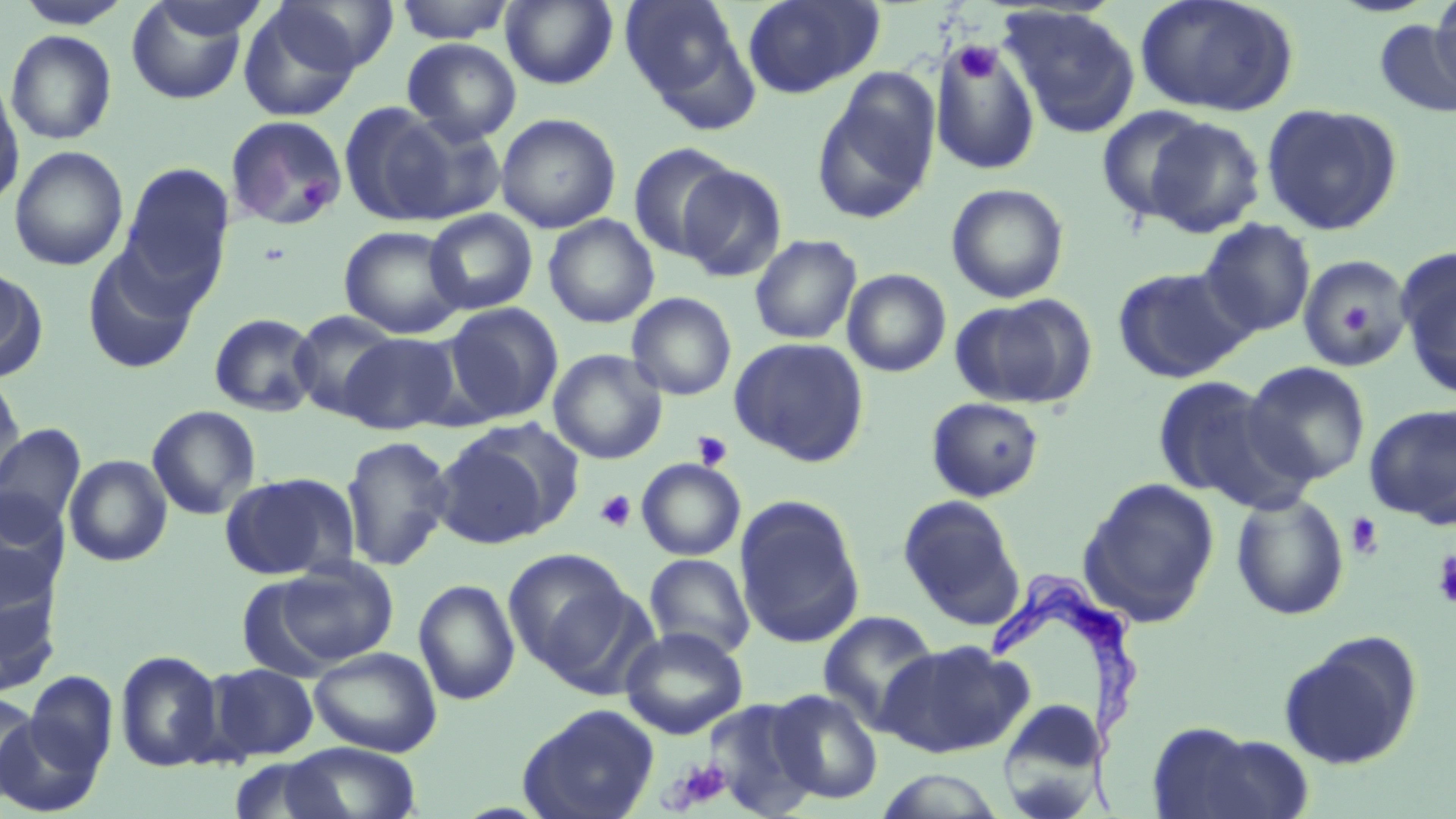
{
  "slide_level_diagnosis": "Trypanosoma brucei",
  "stain": "May-Grünwald-Giemsa",
  "image_size": "1456×819 pixels",
  "field_of_view": "one of a larger specimen",
  "modality": "light microscopy",
  "trypanosoma_brucei_locations": "approximate bounding boxes as [x1, y1, x2, y2] in pixels: [987, 569, 1151, 812]",
  "preparation": "thin blood film",
  "platelet_locations": "approximate bounding boxes as [x1, y1, x2, y2] in pixels: [953, 42, 1002, 84], [298, 175, 338, 211], [1340, 304, 1370, 334], [692, 430, 733, 470], [594, 489, 637, 533], [1345, 514, 1384, 559], [1431, 549, 1456, 609], [669, 758, 733, 810]",
  "magnification": "1000x",
  "uninfected_red_blood_cell_locations": "approximate bounding boxes as [x1, y1, x2, y2] in pixels: [14, 0, 134, 29], [147, 0, 272, 41], [393, 0, 516, 43], [501, 0, 618, 89], [620, 0, 753, 115], [742, 0, 884, 98], [1136, 0, 1297, 117], [1429, 0, 1456, 98], [125, 1, 254, 105], [270, 1, 398, 76], [238, 3, 363, 121], [1001, 5, 1141, 138], [1376, 19, 1456, 118], [4, 29, 117, 145], [402, 38, 522, 144], [931, 43, 1040, 176], [813, 74, 939, 224], [0, 76, 23, 210], [1261, 103, 1402, 235], [341, 104, 469, 226], [1095, 105, 1214, 224], [495, 113, 621, 233], [226, 115, 347, 230], [1144, 117, 1266, 238], [628, 142, 740, 261], [9, 145, 129, 271], [119, 162, 234, 297], [677, 164, 787, 282], [945, 183, 1069, 304], [424, 209, 538, 315], [543, 215, 659, 328], [1198, 219, 1316, 338], [338, 225, 466, 339], [749, 233, 862, 344], [82, 246, 201, 375], [1396, 250, 1456, 399], [1298, 252, 1414, 373], [0, 263, 46, 380], [1112, 265, 1253, 384], [842, 268, 952, 377], [627, 292, 737, 401], [951, 297, 1091, 408], [442, 303, 563, 424], [289, 310, 401, 419], [209, 312, 321, 417], [339, 333, 460, 434], [730, 336, 870, 466], [548, 349, 667, 464], [1242, 361, 1372, 486], [0, 371, 26, 495], [1150, 375, 1295, 506], [926, 397, 1045, 502], [1363, 402, 1456, 528], [146, 404, 261, 520], [0, 423, 87, 536], [435, 423, 575, 545], [340, 434, 455, 572], [64, 454, 172, 567], [637, 458, 746, 560], [219, 472, 359, 581], [1080, 478, 1220, 624], [1230, 490, 1350, 621], [0, 492, 69, 609], [898, 495, 1024, 628], [734, 496, 865, 648], [502, 547, 635, 678], [644, 554, 755, 660], [274, 557, 399, 667], [0, 577, 62, 698], [413, 579, 521, 705], [818, 610, 941, 731], [620, 626, 748, 740], [1279, 632, 1422, 770], [877, 640, 1028, 758], [310, 647, 442, 757], [115, 650, 225, 773], [206, 663, 319, 761], [23, 672, 118, 779], [767, 689, 883, 804], [0, 692, 40, 802], [998, 698, 1102, 814], [702, 699, 820, 817], [517, 703, 660, 819], [2, 708, 104, 817], [1143, 721, 1300, 819], [282, 742, 423, 819], [226, 755, 348, 818], [873, 770, 1007, 818]"
}